Give the extent of all white blood cells.
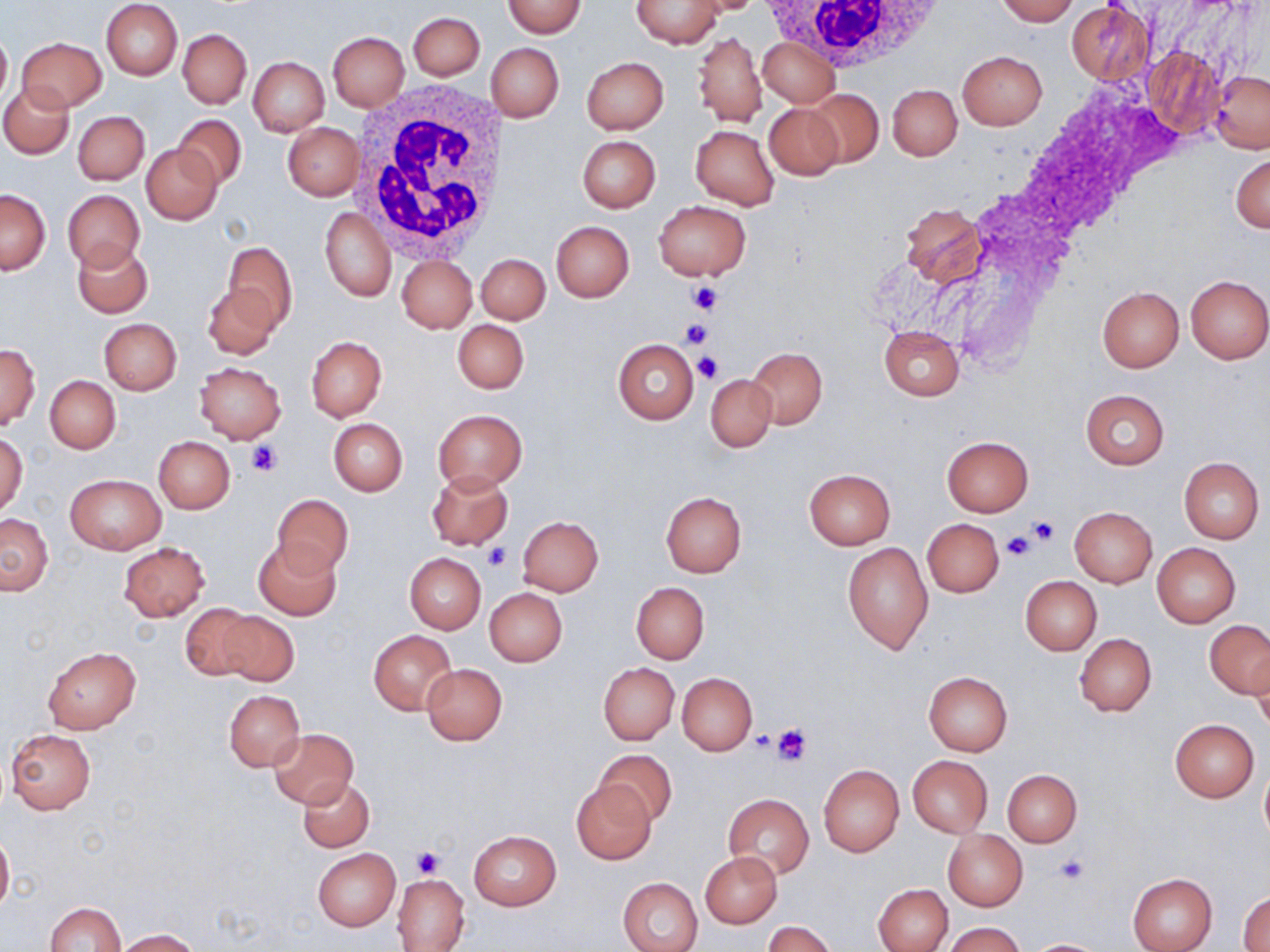

Approximate bounding boxes as (x1,y1)-(x2,y2) corner pairs in pixels.
White blood cells: (757,0)-(949,72), (347,83)-(512,260).

Platelet locations: (689,281)-(722,314), (679,318)-(712,349), (694,352)-(723,383), (249,443)-(281,475), (1025,515)-(1062,545), (1010,520)-(1053,554), (1001,532)-(1035,561), (481,543)-(510,571), (771,722)-(812,766), (410,847)-(444,878), (1052,854)-(1088,886). Uninfected red blood cell locations: (683,0)-(765,15), (995,0)-(1077,24), (101,1)-(182,80), (501,1)-(586,38), (632,1)-(725,48), (1066,2)-(1155,84), (408,11)-(484,80), (0,26)-(11,109), (178,28)-(251,108), (328,31)-(409,111), (694,31)-(767,128), (758,36)-(839,108), (16,38)-(106,113), (487,44)-(564,122), (1144,48)-(1224,136), (958,51)-(1047,129), (248,57)-(329,137), (581,57)-(668,134), (1210,71)-(1270,153), (0,83)-(73,158), (887,84)-(962,160), (807,89)-(884,168), (764,103)-(845,181), (73,111)-(149,185), (173,114)-(246,192), (282,122)-(363,200), (691,125)-(779,210), (577,135)-(661,213), (140,143)-(223,225), (1231,152)-(1270,234), (0,188)-(51,274), (62,189)-(145,272), (654,201)-(750,281), (900,202)-(985,288), (320,208)-(395,301), (550,220)-(634,301), (74,241)-(152,318), (218,241)-(298,334), (476,253)-(550,324), (396,255)-(477,333), (1185,275)-(1270,363), (202,283)-(280,359), (1098,286)-(1184,372), (98,318)-(181,395), (452,319)-(529,394), (878,325)-(964,401), (305,336)-(386,421), (613,340)-(699,423), (0,345)-(40,429), (746,347)-(827,429), (194,362)-(286,443), (705,373)-(777,452), (45,375)-(120,452), (1080,389)-(1169,470), (432,408)-(528,494), (329,418)-(408,496), (0,431)-(27,517), (154,436)-(235,513), (942,436)-(1033,515), (1178,457)-(1264,543), (803,469)-(896,549), (427,470)-(514,548), (65,473)-(166,553), (659,491)-(747,578), (271,494)-(354,578), (1070,506)-(1158,588), (1,514)-(53,595), (517,515)-(602,596), (923,519)-(1003,598), (252,539)-(342,620), (118,541)-(210,621), (841,541)-(932,654), (1152,543)-(1240,627), (404,553)-(486,633), (1020,576)-(1102,655), (631,582)-(708,663), (485,588)-(567,666), (180,603)-(261,680), (215,611)-(299,686), (1204,620)-(1270,698), (368,630)-(458,715), (1073,632)-(1156,716), (43,648)-(140,733), (1252,652)-(1270,736), (421,663)-(507,744), (598,663)-(678,744), (924,671)-(1013,755), (677,672)-(757,755), (225,689)-(305,771), (1170,719)-(1259,801), (270,727)-(359,809), (5,729)-(97,814), (594,749)-(677,826), (908,756)-(993,836), (819,765)-(903,856), (1260,767)-(1270,841), (1004,769)-(1081,847), (298,778)-(374,851), (571,780)-(654,864), (723,793)-(814,878), (0,828)-(13,917), (468,831)-(561,910), (943,831)-(1027,910), (313,848)-(400,930), (701,851)-(782,927), (1127,873)-(1217,952), (393,874)-(469,951), (618,876)-(703,952), (874,883)-(952,952), (1239,890)-(1270,949), (43,902)-(126,952), (762,920)-(835,952), (944,922)-(1024,952), (116,929)-(201,951), (1025,938)-(1112,951). Slide-level diagnosis: negative for blood parasites. May-Grünwald-Giemsa stain. Captured at 1000x magnification. One field of a larger specimen. Thin blood smear. Light microscopy. Image is 1270×952 pixels.